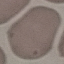
Malaria status: uninfected. Automatically extracted cell patch, resized to 64 × 64 pixels. Thin blood film. Photographed with a smartphone camera at the microscope eyepiece. Giemsa stain.